Comment on the morphology of the erythrocytes.
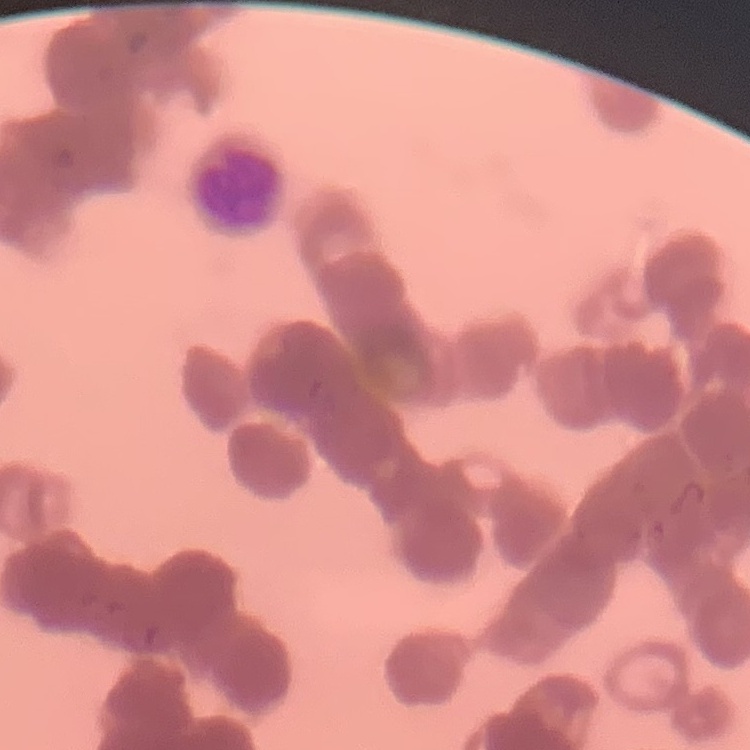
Rouleaux formation.

One tile cut from a larger photomicrograph. Stained with either Field's or Giemsa. Thin blood smear.